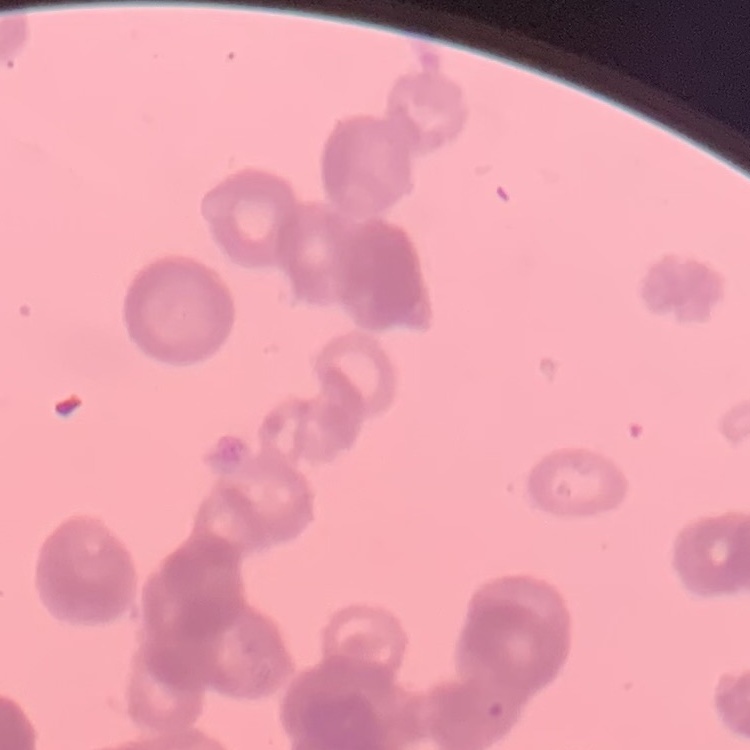

Summary:
  - Red blood cell morphology: rouleaux formation
  - Stain: Field's or Giemsa
  - Preparation: thin blood film
  - Image type: square crop of a larger photomicrograph